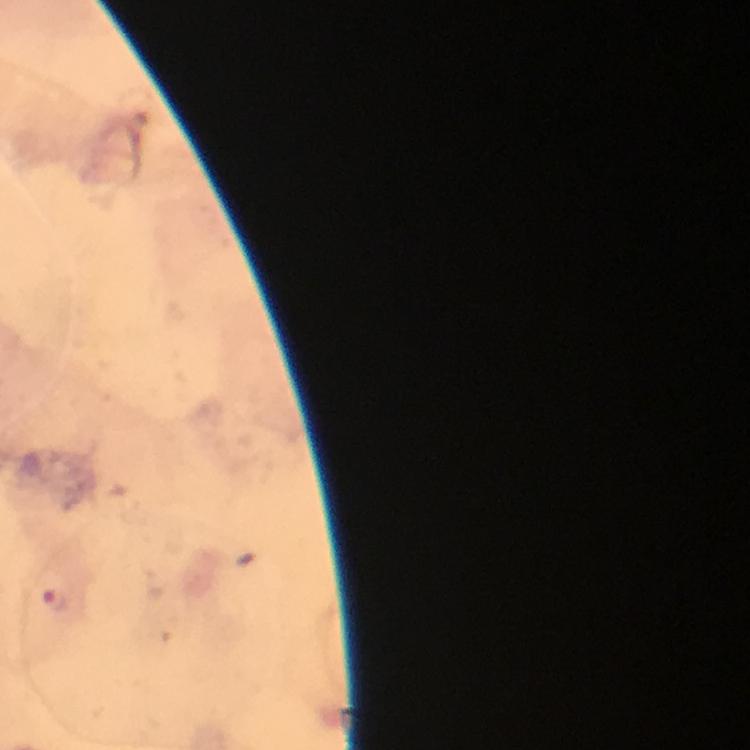
{
  "context": "from a diagnostic examination for malaria",
  "immersion_oil": "applied",
  "preparation": "thick blood smear",
  "stain": "Giemsa",
  "plasmodium_parasite_locations": "approximate centers as {x, y} in pixels: {55, 598}",
  "cropped_from": "a single field of view",
  "image_size": "750×750 pixels",
  "capture": "smartphone camera through the microscope",
  "magnification": "100x"
}